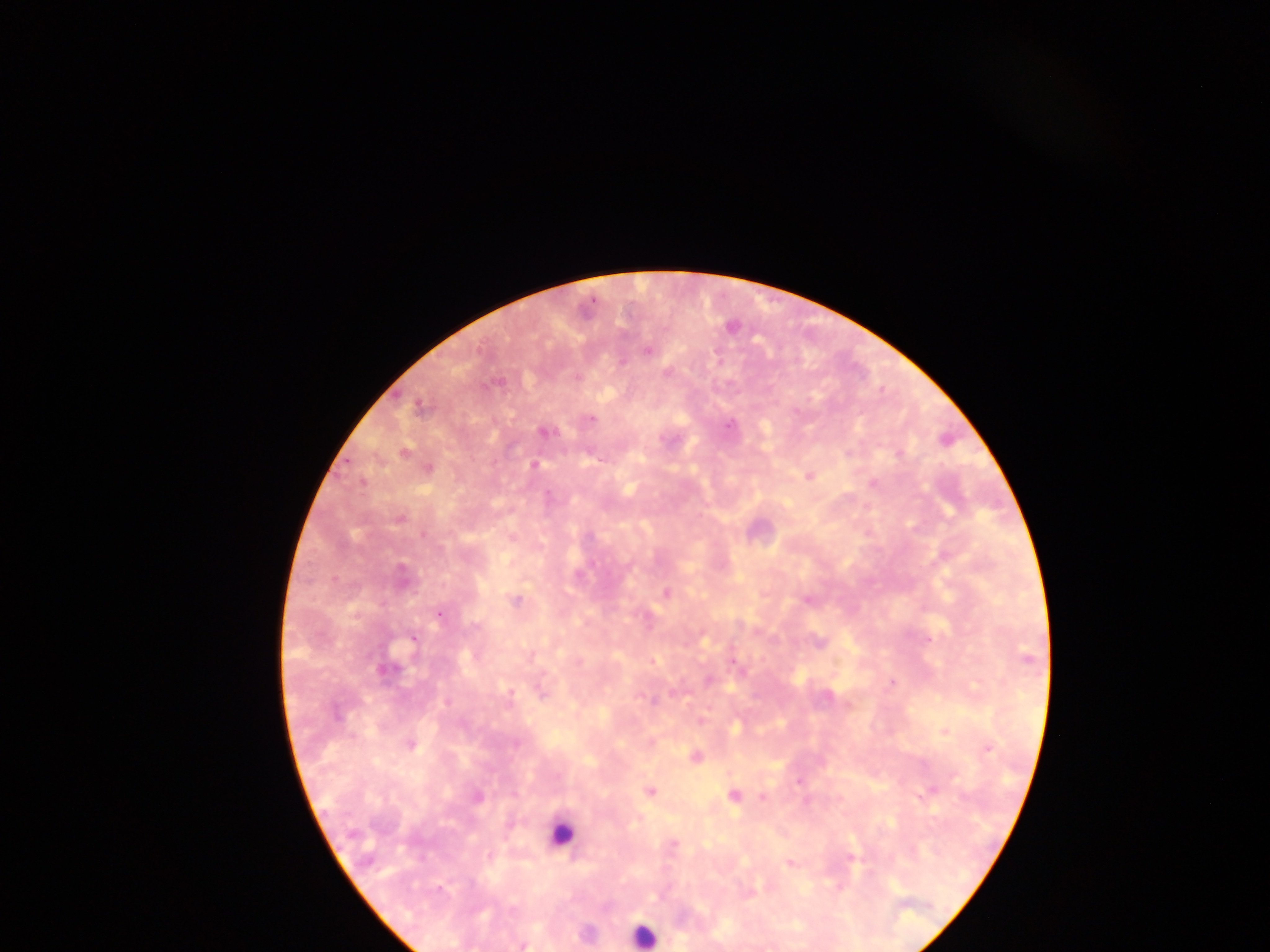

{
  "leukocyte_locations": "approximate centers as x y in pixels: 560 834; 643 935",
  "preparation": "thick blood smear",
  "image_size": "1270×952 pixels",
  "capture": "mobile-phone photograph through a microscope",
  "field_of_view": "single",
  "country": "Ghana",
  "malaria_parasite_locations": "approximate centers as x y in pixels: 731 327; 648 350; 622 362; 667 373; 576 379; 498 381; 419 406; 590 419; 729 425; 545 433; 404 452; 899 453; 535 465; 428 468; 809 476; 363 482; 873 484; 547 495; 400 518; 666 593; 516 601; 806 601; 438 614; 475 627; 411 639; 817 642; 1028 658; 652 661; 732 661; 386 671; 708 679; 891 682; 542 692; 511 694; 336 714; 701 722; 945 731; 410 744; 988 749; 696 756; 798 782; 932 790; 649 791; 734 795; 477 797; 762 797; 674 843; 851 857; 790 864; 441 889; 523 946"
}